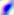
Photomicrograph. 400x magnification. Toxoplasma gondii is seen.